Classify this cell by malaria status.
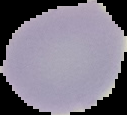

It is uninfected.

Segmented cell region on a black background. From a thin blood film. Image is 127×115 pixels.